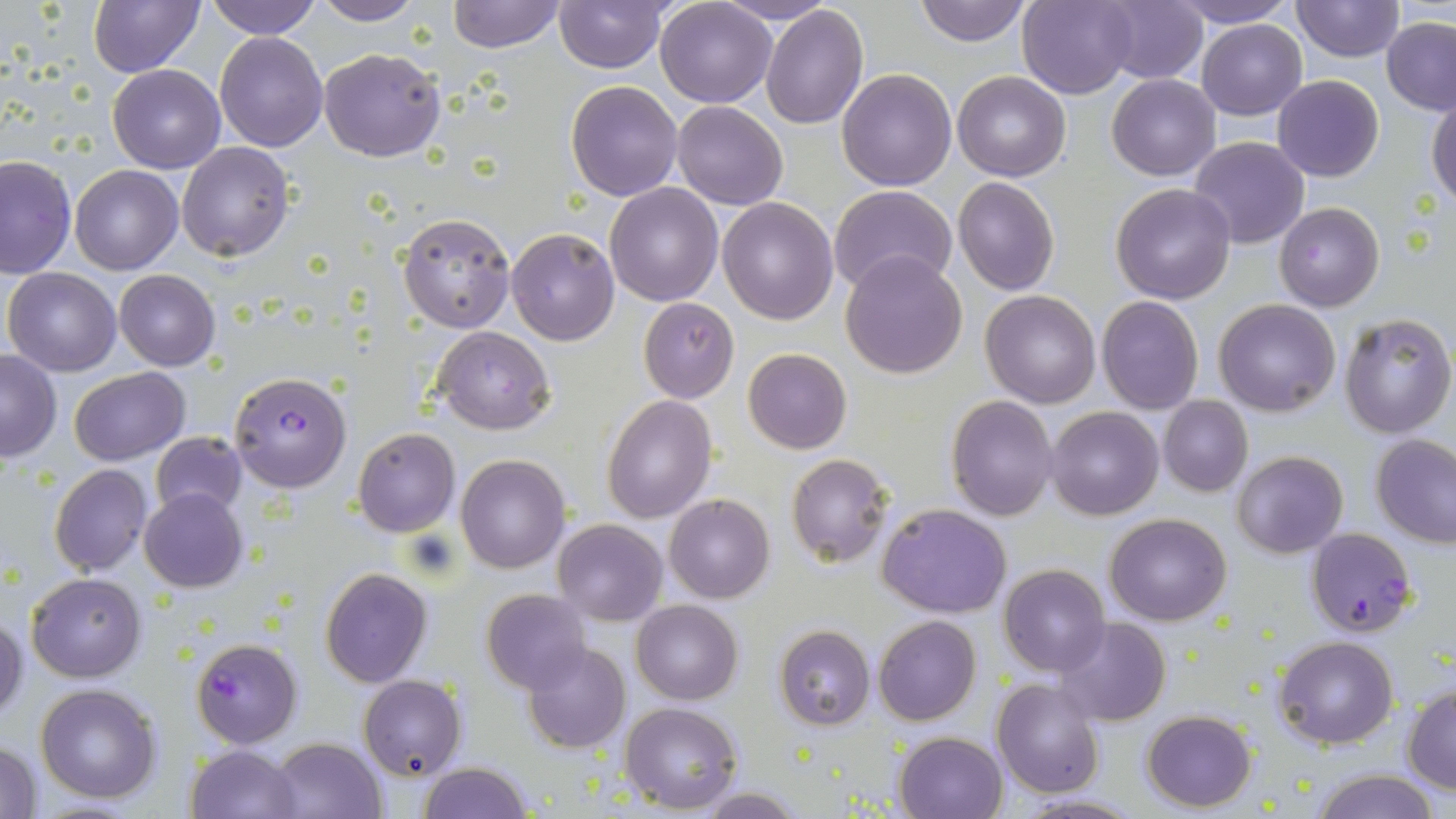
Summary:
  - Coordinate format: approximate bounding boxes as (x1,y1)-(x2,y2) corner pairs in pixels
  - Uninfected red blood cell locations: (88,0)-(203,77), (204,0)-(322,39), (447,0)-(563,52), (655,0)-(776,107), (715,0)-(840,25), (913,0)-(1034,46), (1018,0)-(1138,99), (1161,0)-(1300,27), (1292,0)-(1404,62), (311,1)-(424,25), (554,1)-(669,73), (1094,1)-(1208,85), (759,7)-(869,129), (1380,17)-(1456,115), (1197,19)-(1307,119), (214,32)-(328,151), (320,47)-(445,163), (108,64)-(225,172), (837,68)-(958,190), (952,70)-(1071,182), (1107,74)-(1220,180), (1273,75)-(1384,183), (565,81)-(682,200), (1428,96)-(1456,206), (672,102)-(787,210), (1190,136)-(1309,248), (176,141)-(295,261), (0,155)-(76,279), (69,166)-(183,274), (953,177)-(1059,294), (604,183)-(723,304), (1110,183)-(1236,303), (830,185)-(958,296), (717,198)-(838,325), (1274,203)-(1385,313), (397,211)-(516,333), (506,227)-(619,346), (841,250)-(968,377), (4,267)-(122,376), (114,269)-(220,370), (980,290)-(1102,409), (1096,296)-(1204,415), (638,297)-(739,403), (1213,299)-(1341,417), (1338,313)-(1455,438), (435,325)-(554,435), (742,349)-(852,454), (0,350)-(61,462), (69,366)-(190,465), (603,394)-(716,523), (946,395)-(1060,520), (1158,397)-(1252,496), (1045,406)-(1163,519), (353,428)-(459,537), (151,432)-(247,522), (1372,434)-(1456,547), (1231,450)-(1348,559), (788,454)-(893,568), (456,455)-(570,573), (49,464)-(152,577), (139,487)-(248,592), (664,495)-(774,603), (878,502)-(1012,618), (1105,512)-(1231,625), (552,519)-(668,625), (999,565)-(1110,677), (319,568)-(433,688), (26,573)-(147,681), (481,590)-(591,694), (632,600)-(742,704), (0,613)-(25,724), (873,614)-(982,725), (1055,618)-(1172,726), (774,625)-(875,729), (1274,636)-(1398,748), (522,643)-(631,753), (359,675)-(466,778), (991,678)-(1104,798), (36,683)-(161,804), (1404,685)-(1456,793), (621,702)-(744,813), (1141,710)-(1257,810), (894,731)-(1008,819), (270,736)-(388,819), (1,740)-(44,818), (185,743)-(301,819), (418,762)-(534,819), (1310,769)-(1441,819), (696,787)-(805,817), (1008,792)-(1143,819)
  - Plasmodium falciparum-infected red blood cell locations: (228,371)-(352,493), (1308,528)-(1415,638), (190,637)-(302,747)
  - Slide-level diagnosis: Plasmodium falciparum
  - Modality: optical microscopy
  - Stain: May-Grünwald-Giemsa
  - Magnification: 1000x
  - Field of view: one of a larger specimen
  - Image size: 1456×819 pixels
  - Preparation: thin blood smear